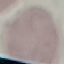
Malaria status: uninfected. Giemsa-stained preparation. Thin smear of blood. Acquired by smartphone through the microscope eyepiece. Automatically extracted cell patch, resized to 64 × 64 pixels.